Identify the parasite.
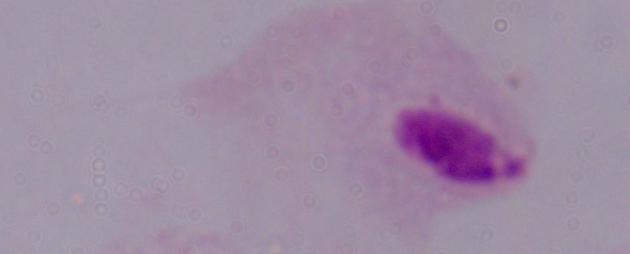

This is a trichomonad.

Summary:
  - Modality: micrograph
  - Magnification: 1000x